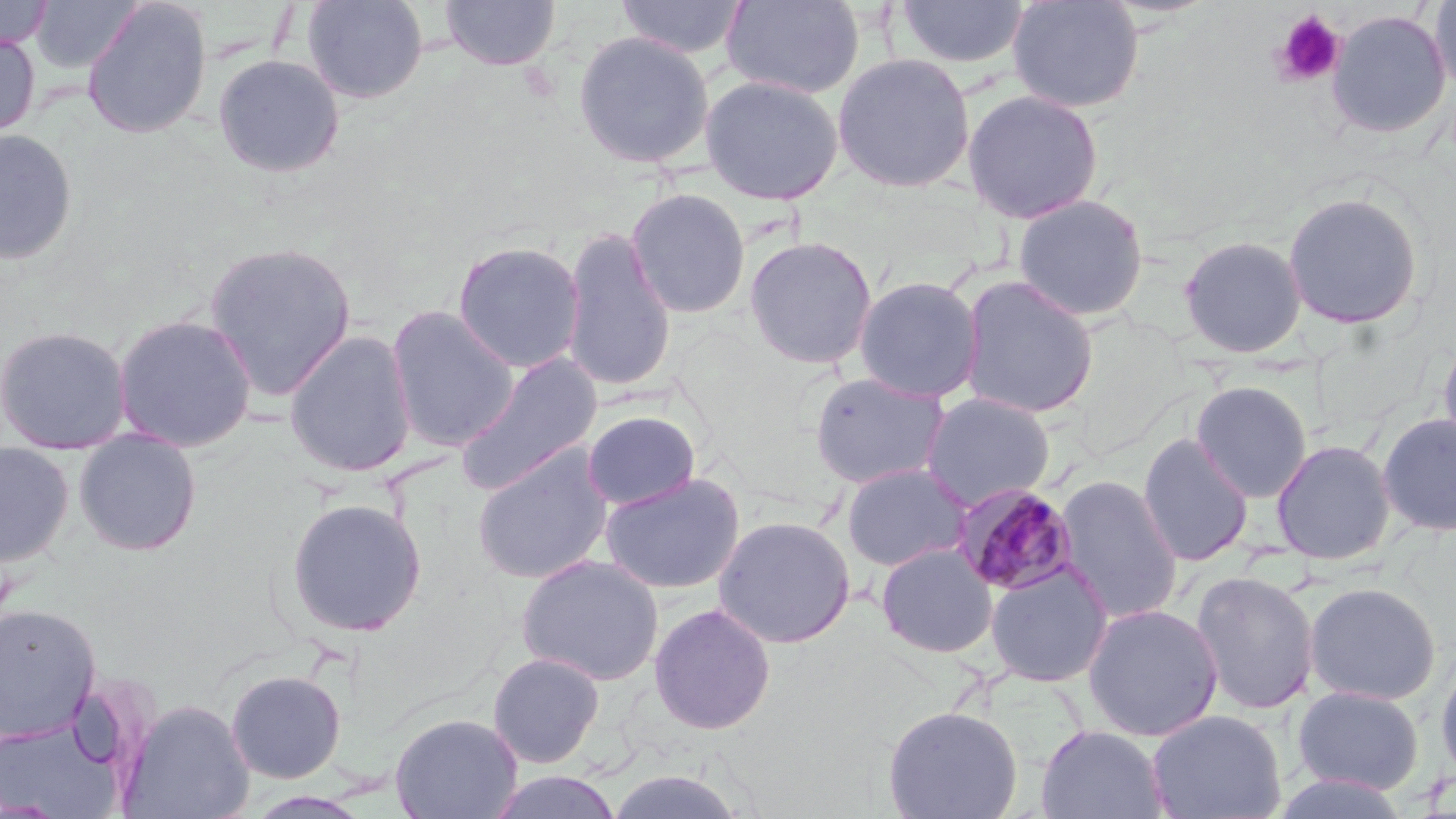
Summary:
  - Coordinate format: approximate bounding boxes as [x1, y1, x2, y2] in pixels
  - Uninfected red blood cell locations: [0, 0, 55, 51], [30, 0, 144, 74], [82, 0, 212, 139], [301, 0, 428, 104], [439, 0, 561, 71], [616, 0, 749, 60], [721, 0, 864, 99], [895, 0, 1030, 70], [1007, 0, 1145, 114], [1428, 1, 1456, 98], [1327, 9, 1452, 140], [0, 29, 41, 139], [573, 30, 714, 169], [832, 52, 976, 193], [212, 53, 346, 178], [699, 74, 844, 205], [962, 89, 1104, 225], [0, 128, 79, 265], [625, 187, 751, 319], [1282, 191, 1424, 330], [1013, 193, 1149, 321], [560, 227, 676, 393], [1178, 234, 1308, 358], [743, 235, 878, 369], [452, 240, 586, 373], [202, 241, 358, 401], [853, 275, 984, 402], [958, 275, 1099, 420], [385, 305, 520, 452], [112, 313, 258, 453], [0, 324, 133, 455], [1437, 328, 1456, 462], [283, 331, 417, 478], [454, 352, 603, 496], [808, 371, 951, 490], [1191, 381, 1312, 502], [920, 392, 1056, 510], [582, 410, 701, 510], [1376, 412, 1456, 536], [72, 429, 203, 556], [1137, 432, 1254, 567], [1270, 439, 1396, 566], [0, 441, 75, 568], [471, 444, 613, 584], [841, 463, 971, 571], [599, 471, 746, 595], [1054, 474, 1183, 624], [286, 498, 427, 638], [713, 515, 856, 649], [876, 542, 998, 658], [516, 554, 664, 686], [985, 561, 1113, 687], [1190, 570, 1321, 716], [1304, 582, 1441, 706], [0, 603, 101, 740], [649, 603, 776, 734], [1082, 603, 1224, 741], [487, 652, 605, 769], [1434, 655, 1456, 786], [226, 669, 347, 783], [1290, 685, 1425, 796], [119, 699, 255, 819], [882, 704, 1023, 819], [1146, 709, 1286, 819], [389, 712, 523, 819], [0, 713, 126, 817], [1036, 724, 1169, 819], [604, 769, 750, 819], [486, 770, 623, 819], [1271, 770, 1412, 818]
  - Platelet locations: [1272, 10, 1346, 86]
  - Plasmodium malariae-infected red blood cell locations: [951, 481, 1081, 597]
  - Slide-level diagnosis: Plasmodium malariae
  - Field of view: single
  - Preparation: thin blood film
  - Magnification: 1000x
  - Image size: 1456×819 pixels
  - Modality: optical microscopy
  - Stain: May-Grünwald-Giemsa